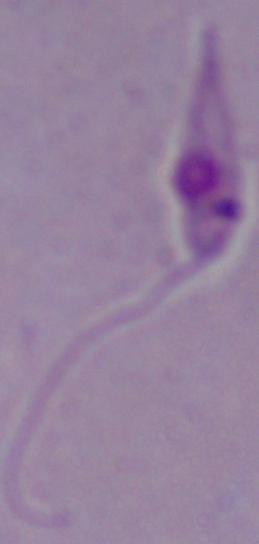

modality = photomicrograph
magnification = 1000x
identification = Leishmania